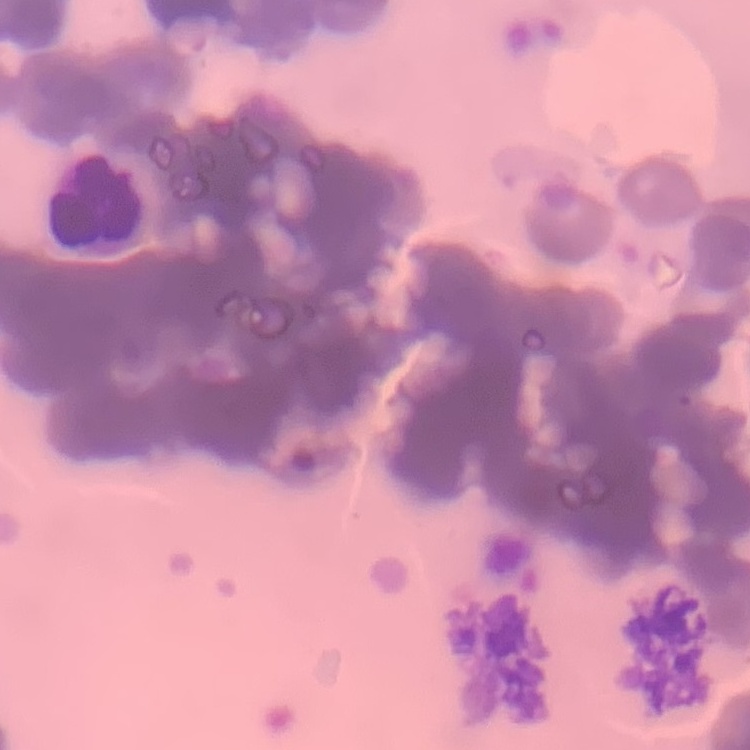

erythrocyte morphology = rouleaux formation
stain = Field's or Giemsa
image type = square crop of a larger photomicrograph
preparation = thin blood smear